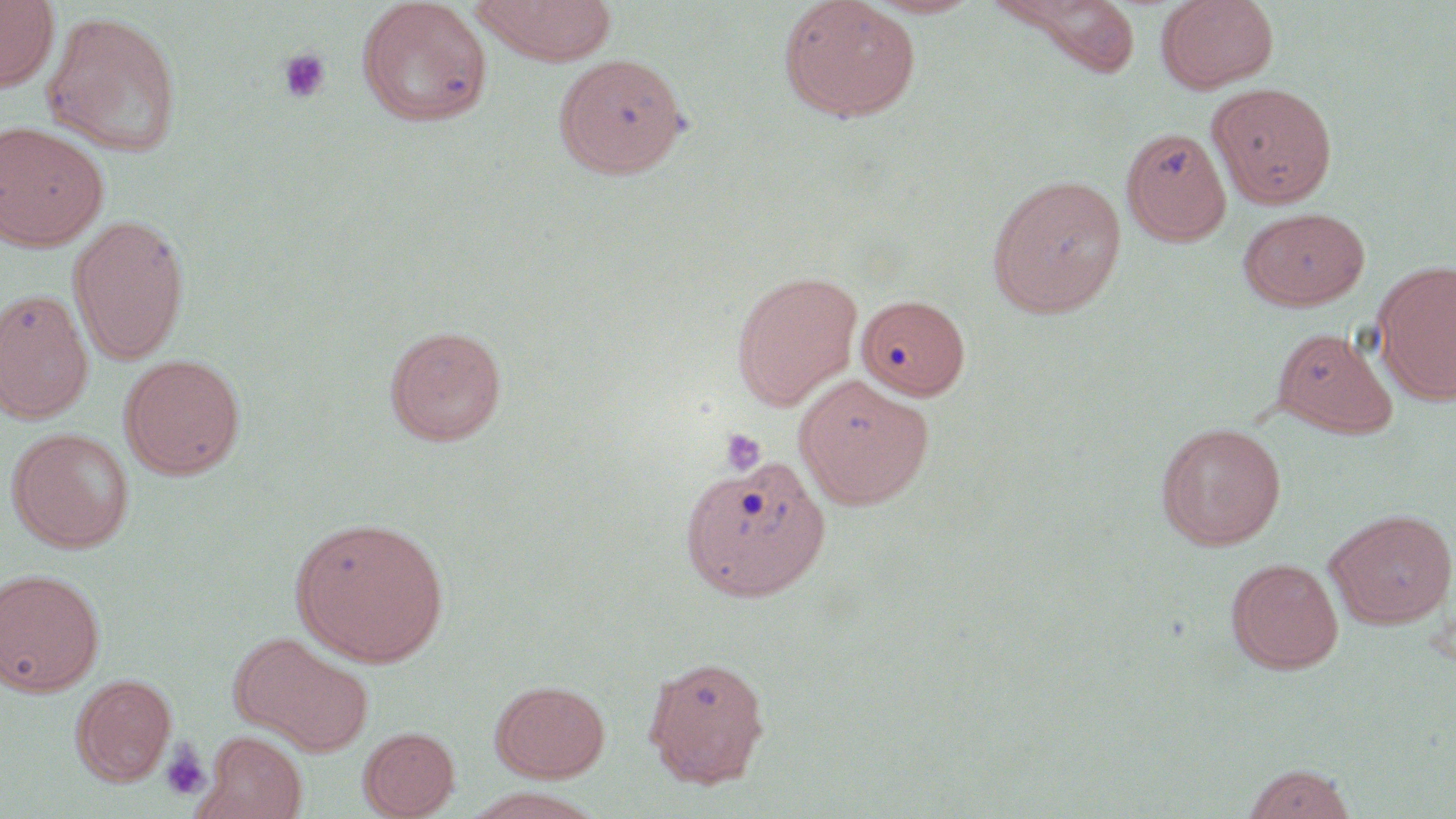
Summary:
  - Coordinate format: approximate bounding boxes as (x1, y1, x2, y2) in pixels
  - Platelet locations: (277, 48, 332, 104), (720, 428, 767, 475), (160, 741, 211, 801)
  - Uninfected red blood cell locations: (0, 0, 59, 92), (471, 0, 618, 65), (778, 0, 922, 122), (863, 0, 982, 19), (1156, 0, 1279, 94), (356, 1, 494, 127), (990, 1, 1143, 77), (41, 10, 183, 157), (554, 53, 690, 178), (1208, 83, 1337, 209), (0, 121, 110, 251), (1121, 125, 1232, 244), (987, 174, 1126, 317), (1239, 206, 1370, 311), (68, 215, 191, 364), (1373, 262, 1456, 404), (730, 270, 863, 410), (0, 289, 93, 423), (856, 294, 970, 400), (384, 324, 508, 447), (1271, 326, 1398, 438), (119, 353, 245, 480), (794, 373, 933, 509), (1155, 422, 1286, 550), (6, 427, 135, 552), (679, 452, 831, 601), (1325, 508, 1456, 628), (289, 514, 450, 666), (1226, 557, 1344, 673), (0, 567, 105, 696), (229, 633, 373, 755), (643, 656, 771, 787), (71, 673, 177, 785), (491, 679, 610, 781), (359, 726, 460, 818), (202, 732, 309, 819), (1241, 763, 1357, 819)
  - Slide-level diagnosis: negative for blood parasites
  - Preparation: thin blood film
  - Modality: optical microscopy
  - Image size: 1456×819 pixels
  - Stain: May-Grünwald-Giemsa
  - Magnification: 1000x
  - Field of view: one of a larger specimen